Report the malaria status of this cell.
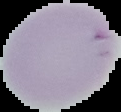
Uninfected.

Summary:
  - Image type: segmented cell region on a black background
  - Image size: 121×112 pixels
  - Preparation: thin blood film